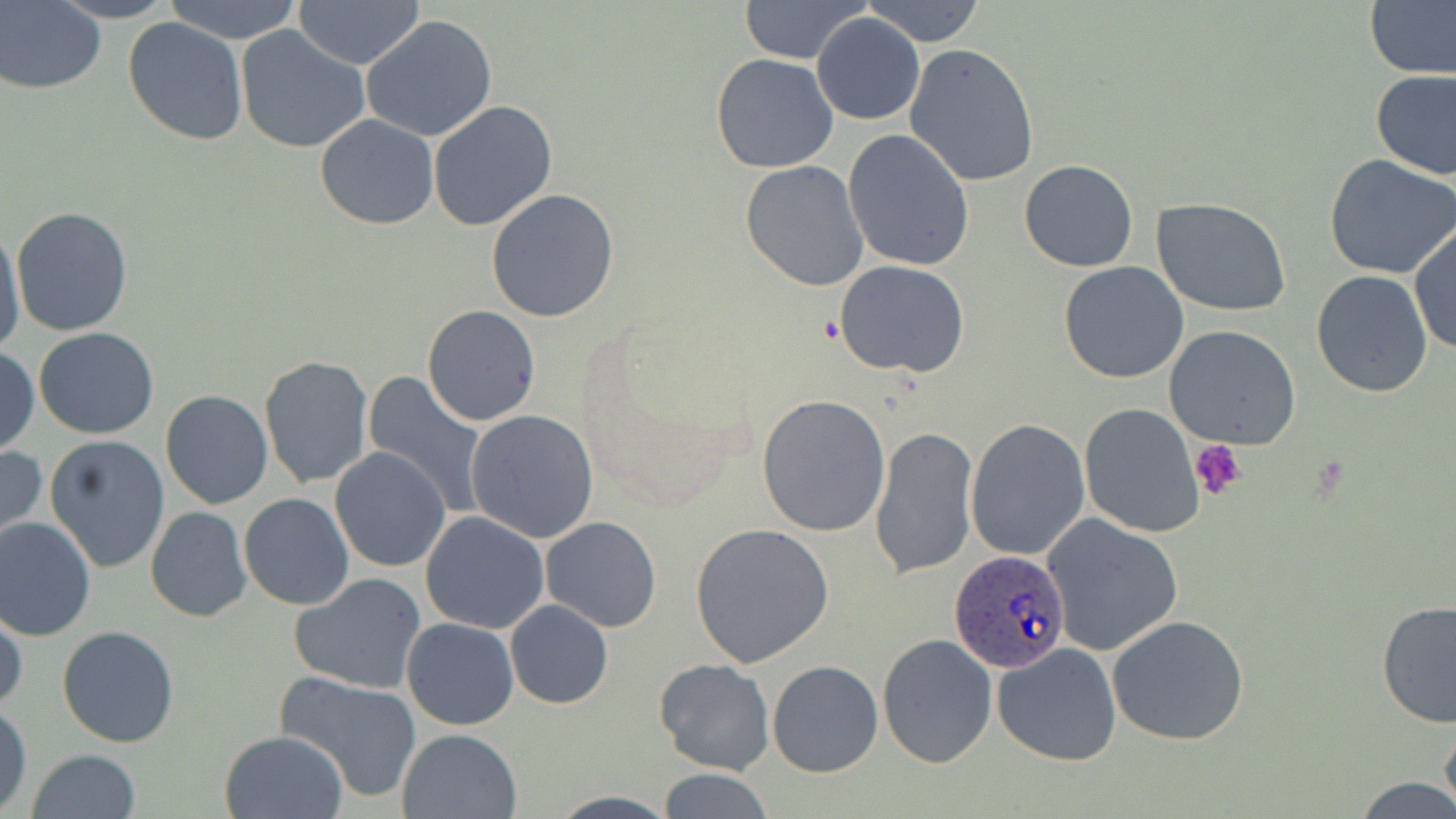
Summary:
  - Coordinate format: approximate bounding boxes as named x1/y1/x2/y2 corners in pixels
  - Platelet locations: (x1=1189, y1=440, x2=1246, y2=501)
  - Uninfected red blood cell locations: (x1=51, y1=0, x2=179, y2=23), (x1=163, y1=0, x2=304, y2=42), (x1=738, y1=0, x2=872, y2=64), (x1=863, y1=0, x2=986, y2=47), (x1=293, y1=1, x2=425, y2=70), (x1=1, y1=2, x2=105, y2=92), (x1=1366, y1=3, x2=1456, y2=79), (x1=359, y1=13, x2=499, y2=141), (x1=812, y1=13, x2=925, y2=125), (x1=121, y1=17, x2=248, y2=146), (x1=235, y1=26, x2=369, y2=153), (x1=903, y1=42, x2=1041, y2=187), (x1=711, y1=53, x2=839, y2=173), (x1=1370, y1=69, x2=1456, y2=180), (x1=428, y1=100, x2=559, y2=232), (x1=314, y1=114, x2=439, y2=229), (x1=842, y1=128, x2=974, y2=271), (x1=1324, y1=155, x2=1456, y2=280), (x1=1019, y1=159, x2=1140, y2=272), (x1=738, y1=160, x2=869, y2=291), (x1=485, y1=189, x2=621, y2=324), (x1=1155, y1=200, x2=1291, y2=316), (x1=10, y1=205, x2=132, y2=336), (x1=0, y1=223, x2=25, y2=360), (x1=1410, y1=223, x2=1455, y2=358), (x1=833, y1=260, x2=969, y2=379), (x1=1059, y1=261, x2=1190, y2=384), (x1=1311, y1=269, x2=1434, y2=397), (x1=422, y1=306, x2=541, y2=426), (x1=1164, y1=325, x2=1301, y2=448), (x1=34, y1=328, x2=159, y2=439), (x1=1, y1=345, x2=38, y2=456), (x1=259, y1=355, x2=373, y2=489), (x1=361, y1=372, x2=491, y2=515), (x1=168, y1=375, x2=366, y2=497), (x1=160, y1=389, x2=272, y2=509), (x1=757, y1=394, x2=891, y2=538), (x1=1078, y1=402, x2=1205, y2=537), (x1=466, y1=408, x2=599, y2=544), (x1=966, y1=419, x2=1090, y2=560), (x1=869, y1=425, x2=979, y2=578), (x1=44, y1=435, x2=171, y2=575), (x1=0, y1=444, x2=47, y2=549), (x1=330, y1=447, x2=451, y2=572), (x1=239, y1=493, x2=355, y2=609), (x1=145, y1=506, x2=252, y2=621), (x1=420, y1=512, x2=549, y2=633), (x1=1042, y1=512, x2=1185, y2=657), (x1=0, y1=516, x2=98, y2=640), (x1=541, y1=516, x2=662, y2=633), (x1=689, y1=523, x2=835, y2=669), (x1=290, y1=573, x2=425, y2=695), (x1=1375, y1=598, x2=1456, y2=731), (x1=1, y1=600, x2=25, y2=717), (x1=505, y1=600, x2=613, y2=709), (x1=1107, y1=615, x2=1250, y2=745), (x1=401, y1=617, x2=520, y2=730), (x1=57, y1=627, x2=181, y2=747), (x1=878, y1=632, x2=999, y2=770), (x1=991, y1=643, x2=1123, y2=767), (x1=655, y1=659, x2=774, y2=776), (x1=767, y1=660, x2=883, y2=777), (x1=274, y1=671, x2=422, y2=803), (x1=0, y1=702, x2=33, y2=816), (x1=1440, y1=712, x2=1456, y2=817), (x1=397, y1=728, x2=522, y2=818), (x1=220, y1=730, x2=348, y2=819), (x1=26, y1=749, x2=141, y2=819), (x1=655, y1=768, x2=776, y2=819), (x1=1353, y1=775, x2=1456, y2=818)
  - Plasmodium ovale-infected red blood cell locations: (x1=951, y1=551, x2=1071, y2=673)
  - Slide-level diagnosis: Plasmodium ovale
  - Modality: light microscopy
  - Preparation: thin blood film
  - Field of view: one of a larger specimen
  - Magnification: 1000x
  - Image size: 1456×819 pixels
  - Stain: May-Grünwald-Giemsa